Outline each blood parasite and name the species.
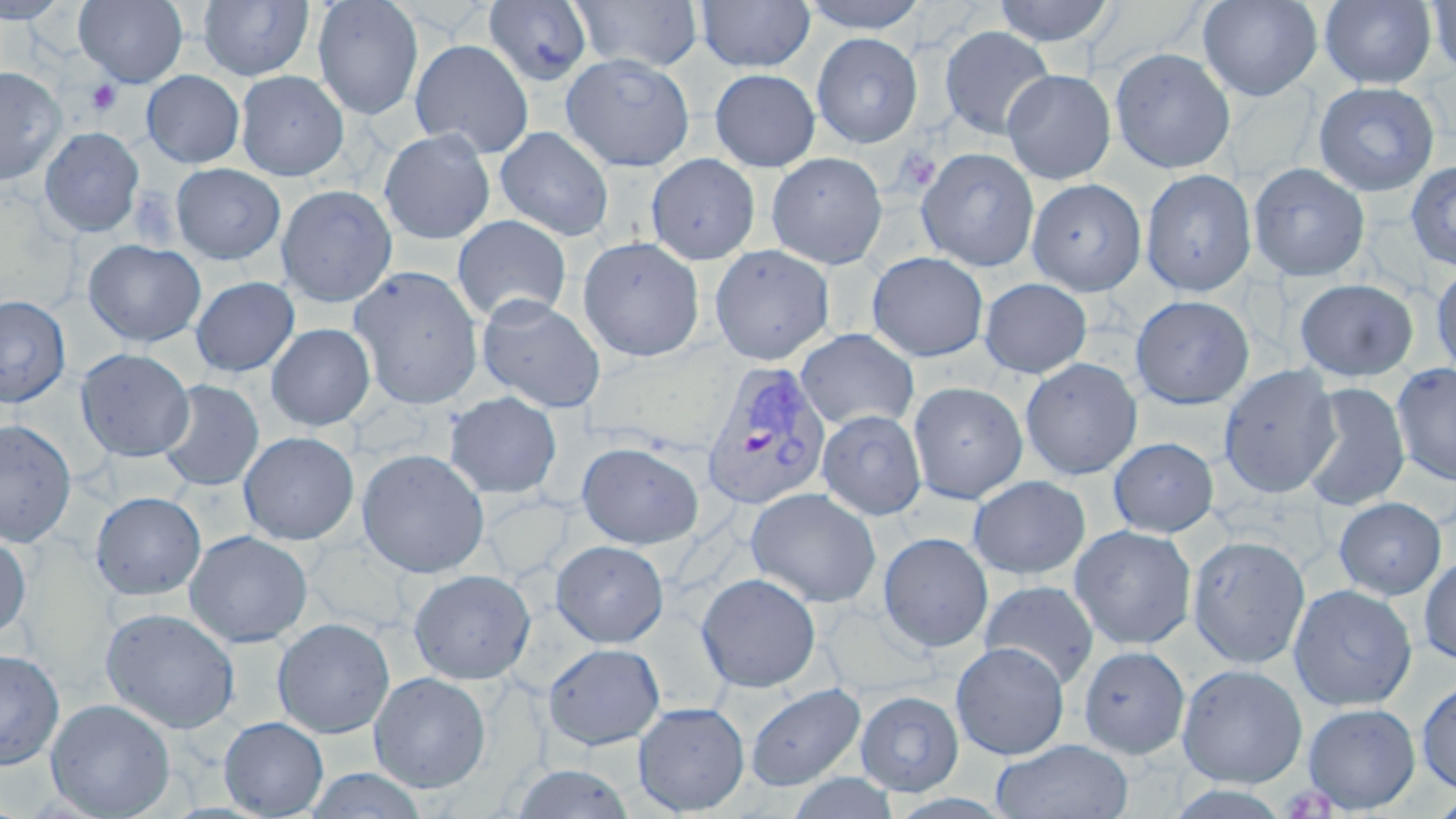
Approximate bounding boxes as named x1/y1/x2/y2 corners in pixels.
Plasmodium vivax-infected red blood cells: (x1=701, y1=360, x2=833, y2=512).
No Plasmodium falciparum, Plasmodium ovale, Plasmodium malariae, Babesia divergens, or Trypanosoma brucei observed.

Summary:
  - Platelet locations: (x1=86, y1=80, x2=122, y2=116), (x1=895, y1=147, x2=942, y2=193), (x1=128, y1=185, x2=181, y2=248)
  - Uninfected red blood cell locations: (x1=0, y1=0, x2=70, y2=23), (x1=73, y1=0, x2=188, y2=87), (x1=198, y1=0, x2=313, y2=81), (x1=312, y1=0, x2=424, y2=120), (x1=695, y1=0, x2=815, y2=73), (x1=799, y1=0, x2=930, y2=33), (x1=992, y1=0, x2=1117, y2=47), (x1=1198, y1=0, x2=1323, y2=102), (x1=483, y1=1, x2=593, y2=86), (x1=570, y1=1, x2=703, y2=73), (x1=1319, y1=1, x2=1437, y2=89), (x1=1426, y1=1, x2=1456, y2=76), (x1=938, y1=25, x2=1055, y2=140), (x1=811, y1=33, x2=923, y2=148), (x1=410, y1=39, x2=534, y2=158), (x1=1110, y1=48, x2=1235, y2=174), (x1=560, y1=52, x2=695, y2=172), (x1=0, y1=66, x2=67, y2=186), (x1=709, y1=69, x2=821, y2=172), (x1=1002, y1=69, x2=1116, y2=184), (x1=141, y1=70, x2=245, y2=168), (x1=236, y1=71, x2=349, y2=181), (x1=1313, y1=81, x2=1440, y2=196), (x1=494, y1=126, x2=614, y2=242), (x1=39, y1=127, x2=145, y2=238), (x1=378, y1=128, x2=496, y2=245), (x1=916, y1=148, x2=1039, y2=272), (x1=766, y1=152, x2=888, y2=269), (x1=645, y1=153, x2=761, y2=265), (x1=1405, y1=161, x2=1456, y2=270), (x1=171, y1=163, x2=286, y2=265), (x1=1248, y1=163, x2=1370, y2=282), (x1=1140, y1=169, x2=1257, y2=297), (x1=1026, y1=178, x2=1147, y2=295), (x1=276, y1=185, x2=397, y2=307), (x1=451, y1=215, x2=571, y2=325), (x1=577, y1=235, x2=705, y2=362), (x1=83, y1=239, x2=206, y2=347), (x1=709, y1=245, x2=835, y2=365), (x1=866, y1=251, x2=989, y2=362), (x1=1430, y1=263, x2=1456, y2=380), (x1=349, y1=266, x2=485, y2=410), (x1=190, y1=277, x2=299, y2=377), (x1=979, y1=277, x2=1092, y2=378), (x1=1294, y1=278, x2=1419, y2=382), (x1=0, y1=295, x2=71, y2=407), (x1=476, y1=295, x2=607, y2=414), (x1=1130, y1=295, x2=1254, y2=409), (x1=266, y1=323, x2=376, y2=431), (x1=255, y1=324, x2=365, y2=544), (x1=795, y1=328, x2=919, y2=432), (x1=76, y1=348, x2=194, y2=462), (x1=1020, y1=358, x2=1142, y2=480), (x1=1391, y1=363, x2=1456, y2=487), (x1=1218, y1=364, x2=1340, y2=498), (x1=157, y1=379, x2=264, y2=492), (x1=908, y1=381, x2=1028, y2=504), (x1=1299, y1=383, x2=1410, y2=511), (x1=444, y1=391, x2=562, y2=499), (x1=817, y1=410, x2=927, y2=520), (x1=0, y1=418, x2=76, y2=548), (x1=238, y1=432, x2=360, y2=545), (x1=1107, y1=437, x2=1219, y2=538), (x1=576, y1=441, x2=704, y2=549), (x1=356, y1=448, x2=489, y2=578), (x1=967, y1=475, x2=1091, y2=580), (x1=746, y1=488, x2=882, y2=608), (x1=90, y1=491, x2=207, y2=600), (x1=1333, y1=497, x2=1447, y2=600), (x1=1068, y1=525, x2=1197, y2=650), (x1=184, y1=530, x2=313, y2=648), (x1=0, y1=532, x2=31, y2=641), (x1=878, y1=532, x2=994, y2=653), (x1=1187, y1=535, x2=1310, y2=669), (x1=550, y1=540, x2=669, y2=648), (x1=1418, y1=555, x2=1456, y2=665), (x1=409, y1=569, x2=536, y2=684), (x1=696, y1=572, x2=821, y2=692), (x1=979, y1=580, x2=1099, y2=690), (x1=1288, y1=584, x2=1417, y2=711), (x1=101, y1=607, x2=240, y2=735), (x1=272, y1=618, x2=395, y2=739), (x1=951, y1=641, x2=1069, y2=760), (x1=543, y1=642, x2=665, y2=750), (x1=1078, y1=645, x2=1190, y2=760), (x1=0, y1=649, x2=64, y2=769), (x1=1176, y1=663, x2=1308, y2=788), (x1=369, y1=672, x2=491, y2=792), (x1=1416, y1=676, x2=1456, y2=794), (x1=745, y1=683, x2=866, y2=792), (x1=855, y1=690, x2=964, y2=795), (x1=45, y1=698, x2=176, y2=818), (x1=632, y1=702, x2=750, y2=815), (x1=1301, y1=702, x2=1421, y2=813), (x1=218, y1=716, x2=329, y2=818), (x1=991, y1=737, x2=1133, y2=819), (x1=509, y1=764, x2=637, y2=819), (x1=304, y1=768, x2=429, y2=818), (x1=786, y1=771, x2=899, y2=818), (x1=1430, y1=794, x2=1456, y2=818)
  - Slide-level diagnosis: Plasmodium vivax
  - Field of view: one of a larger specimen
  - Modality: light microscopy
  - Image size: 1456×819 pixels
  - Stain: May-Grünwald-Giemsa
  - Magnification: 1000x
  - Preparation: thin blood smear